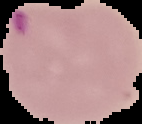 Image is 142×124 pixels. The area outside the segmented cell region is set to black. Malaria status: parasitized. From a thin blood smear.